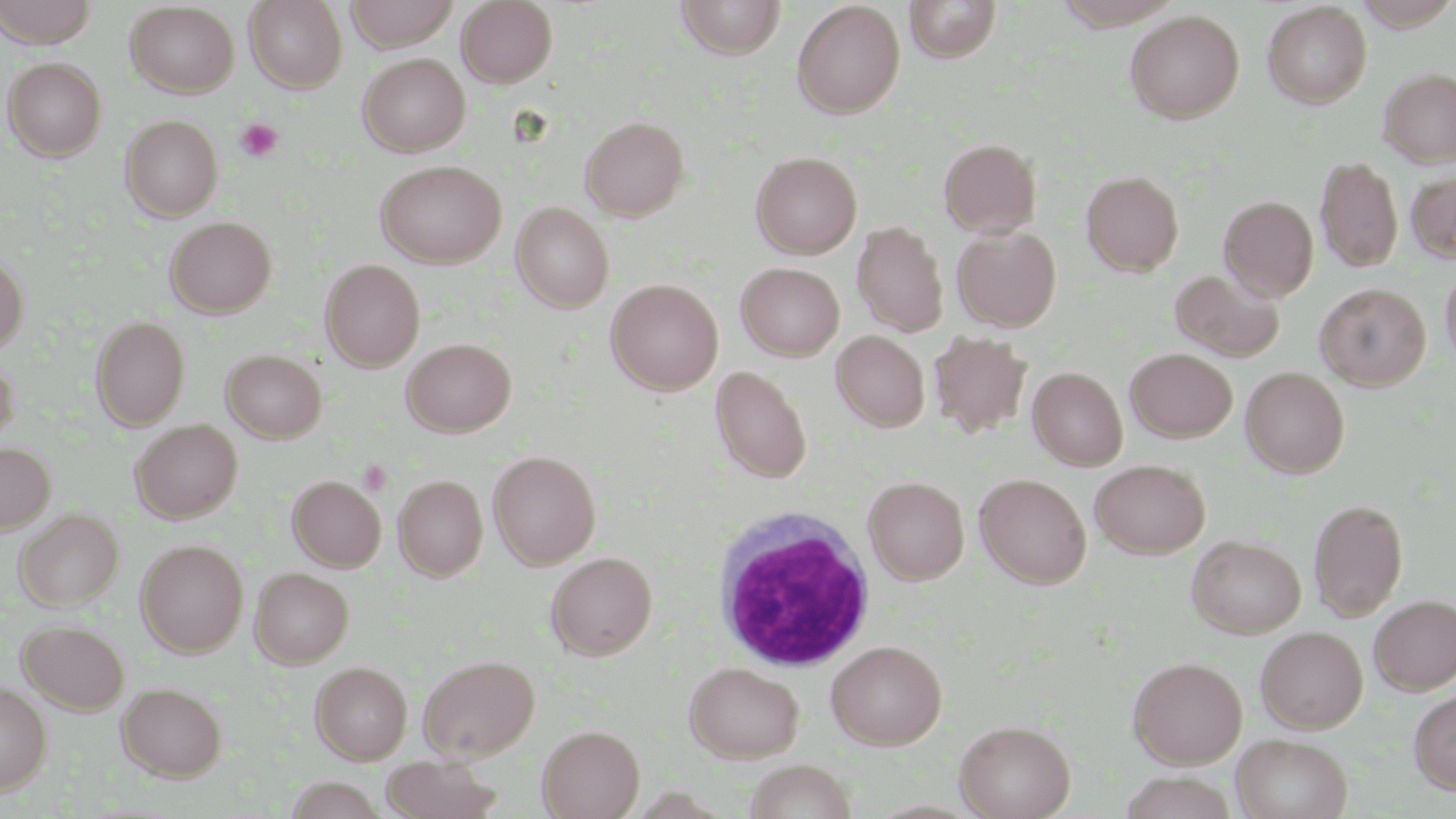

slide-level diagnosis = no evidence of blood parasites
stain = May-Grünwald-Giemsa
modality = optical microscopy
magnification = 1000x
platelet locations = approximate bounding boxes as named x1/y1/x2/y2 corners in pixels: (x1=237, y1=118, x2=282, y2=161), (x1=359, y1=460, x2=392, y2=495)
preparation = thin blood smear
image size = 1456×819 pixels
uninfected red blood cell locations = approximate bounding boxes as named x1/y1/x2/y2 corners in pixels: (x1=1, y1=0, x2=98, y2=47), (x1=244, y1=0, x2=348, y2=93), (x1=344, y1=0, x2=459, y2=50), (x1=456, y1=0, x2=557, y2=87), (x1=675, y1=0, x2=786, y2=59), (x1=904, y1=0, x2=1002, y2=62), (x1=792, y1=1, x2=905, y2=118), (x1=1352, y1=1, x2=1456, y2=30), (x1=1261, y1=2, x2=1372, y2=108), (x1=125, y1=3, x2=239, y2=97), (x1=1124, y1=9, x2=1245, y2=124), (x1=358, y1=52, x2=470, y2=156), (x1=2, y1=56, x2=106, y2=160), (x1=1378, y1=67, x2=1456, y2=168), (x1=120, y1=115, x2=222, y2=221), (x1=580, y1=115, x2=689, y2=220), (x1=938, y1=138, x2=1041, y2=238), (x1=751, y1=151, x2=861, y2=259), (x1=1315, y1=156, x2=1403, y2=272), (x1=375, y1=159, x2=507, y2=268), (x1=1406, y1=168, x2=1456, y2=264), (x1=1081, y1=170, x2=1184, y2=275), (x1=1219, y1=195, x2=1318, y2=300), (x1=511, y1=202, x2=614, y2=313), (x1=165, y1=216, x2=277, y2=318), (x1=852, y1=221, x2=949, y2=337), (x1=952, y1=225, x2=1062, y2=331), (x1=0, y1=253, x2=28, y2=353), (x1=320, y1=259, x2=424, y2=371), (x1=1440, y1=261, x2=1456, y2=368), (x1=736, y1=262, x2=844, y2=360), (x1=1170, y1=269, x2=1284, y2=362), (x1=606, y1=278, x2=723, y2=395), (x1=1316, y1=283, x2=1430, y2=389), (x1=90, y1=316, x2=190, y2=429), (x1=831, y1=330, x2=930, y2=431), (x1=929, y1=331, x2=1031, y2=438), (x1=402, y1=338, x2=516, y2=436), (x1=1125, y1=347, x2=1237, y2=442), (x1=222, y1=349, x2=326, y2=442), (x1=0, y1=357, x2=19, y2=449), (x1=710, y1=365, x2=812, y2=483), (x1=1028, y1=366, x2=1127, y2=470), (x1=1241, y1=366, x2=1350, y2=477), (x1=131, y1=419, x2=242, y2=523), (x1=0, y1=442, x2=55, y2=534), (x1=488, y1=450, x2=601, y2=569), (x1=1090, y1=459, x2=1210, y2=558), (x1=974, y1=473, x2=1092, y2=588), (x1=394, y1=474, x2=487, y2=580), (x1=288, y1=475, x2=385, y2=571), (x1=863, y1=475, x2=969, y2=585), (x1=1308, y1=498, x2=1408, y2=620), (x1=14, y1=508, x2=123, y2=610), (x1=1187, y1=535, x2=1306, y2=638), (x1=136, y1=539, x2=248, y2=656), (x1=546, y1=551, x2=657, y2=660), (x1=250, y1=567, x2=353, y2=667), (x1=1370, y1=594, x2=1456, y2=693), (x1=19, y1=619, x2=129, y2=714), (x1=1255, y1=626, x2=1368, y2=733), (x1=826, y1=640, x2=947, y2=750), (x1=418, y1=654, x2=540, y2=761), (x1=1128, y1=656, x2=1248, y2=768), (x1=309, y1=661, x2=412, y2=764), (x1=684, y1=662, x2=804, y2=763), (x1=0, y1=680, x2=51, y2=794), (x1=117, y1=681, x2=227, y2=781), (x1=1409, y1=689, x2=1456, y2=795), (x1=954, y1=719, x2=1075, y2=819), (x1=537, y1=725, x2=645, y2=819), (x1=1231, y1=733, x2=1352, y2=819), (x1=380, y1=753, x2=503, y2=819), (x1=743, y1=759, x2=858, y2=819), (x1=1116, y1=770, x2=1239, y2=818)
white blood cell locations = approximate bounding boxes as named x1/y1/x2/y2 corners in pixels: (x1=712, y1=508, x2=876, y2=673)
field of view = single